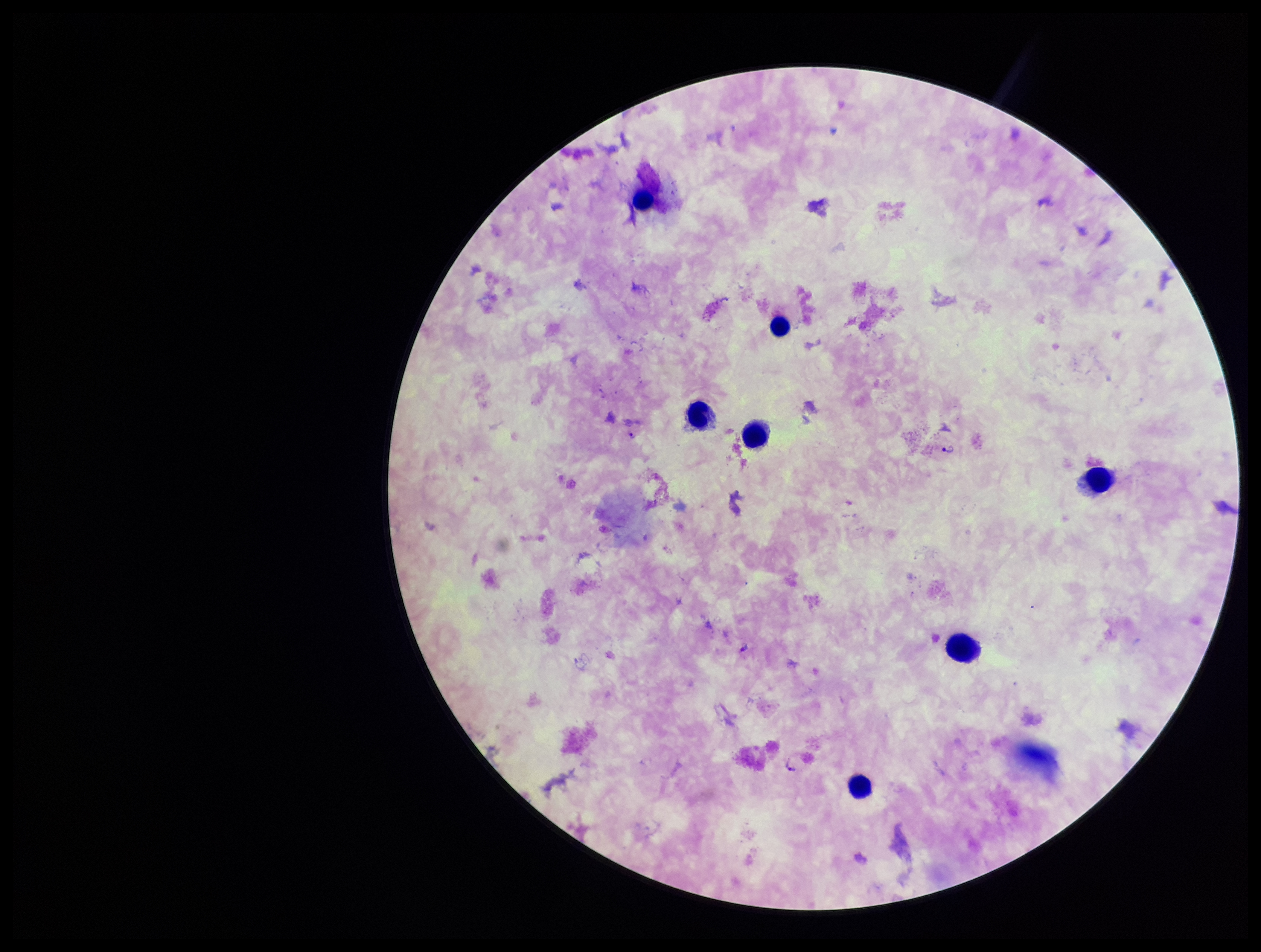

Stained with Giemsa. Species reported for this patient: Plasmodium falciparum. Image is 1261×952 pixels. Preparation: thick blood smear. Plasmodium parasites: seen. Parasite count: 4. Single field of view. Patient malaria status: positive. Leukocyte count: 7. Smartphone photograph taken through the eyepiece of a microscope.